Locate every malaria parasite and every leukocyte.
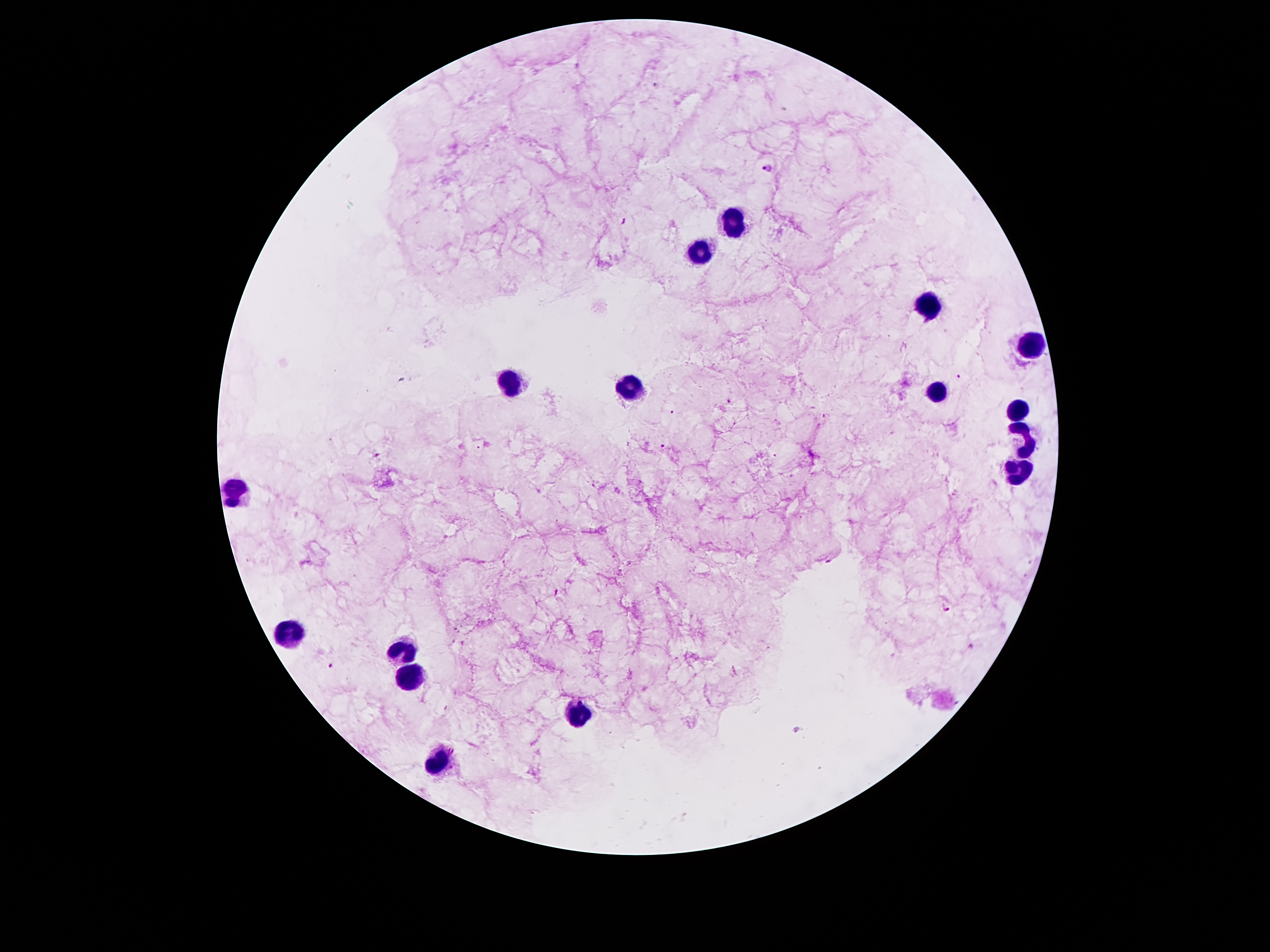
Approximate object centers, in pixels from the top-left corner.
Malaria parasites: (x=767, y=167), (x=624, y=222), (x=960, y=376), (x=729, y=402), (x=673, y=412), (x=663, y=446), (x=377, y=455), (x=947, y=610), (x=331, y=666).
Leukocytes: (x=731, y=217), (x=697, y=252), (x=929, y=303), (x=1030, y=346), (x=509, y=381), (x=628, y=394), (x=936, y=394), (x=1017, y=411), (x=1026, y=441), (x=1019, y=471), (x=236, y=489), (x=292, y=634), (x=404, y=648), (x=408, y=678), (x=580, y=714), (x=436, y=762).

Summary:
  - Magnification: 100x
  - Field of view: one from this slide
  - Capture: smartphone through the microscope eyepiece
  - Preparation: thick blood film
  - Stain: Giemsa
  - Patient malaria status: positive for Plasmodium falciparum
  - Image size: 1270×952 pixels